Assess this cell for malaria.
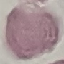
Uninfected.

Acquired by smartphone through the microscope eyepiece. Giemsa stain. Thin blood smear. Automatically extracted cell patch, resized to 64 × 64 pixels.